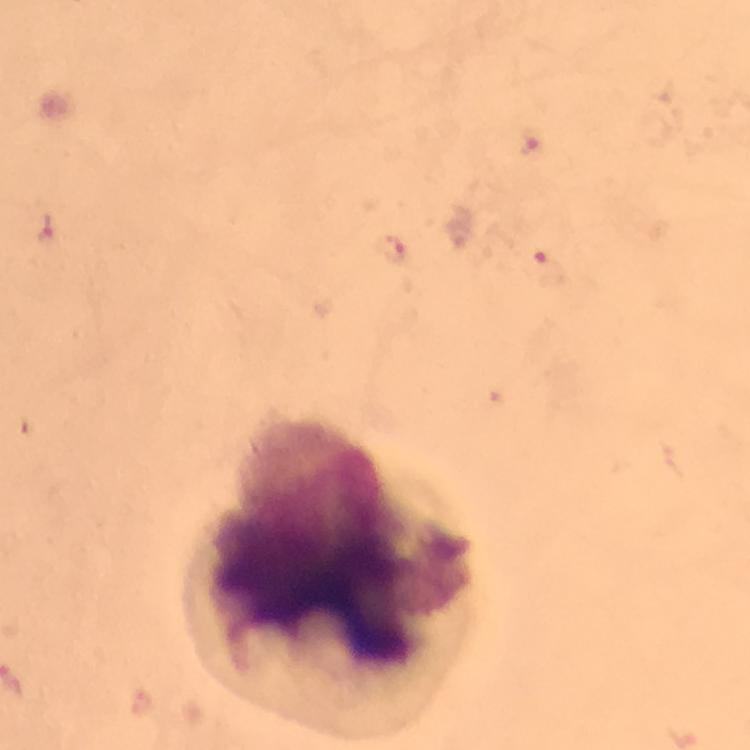
stain = Giemsa
context = from a diagnostic examination for malaria
magnification = 100x
capture = smartphone camera through the microscope
cropped from = one field of view
image size = 750×750 pixels
preparation = thick blood smear
immersion oil = applied
malaria parasite locations = approximate centers as {x, y} in pixels: {531, 147}, {47, 229}, {390, 253}, {546, 269}